State the blood parasite species.
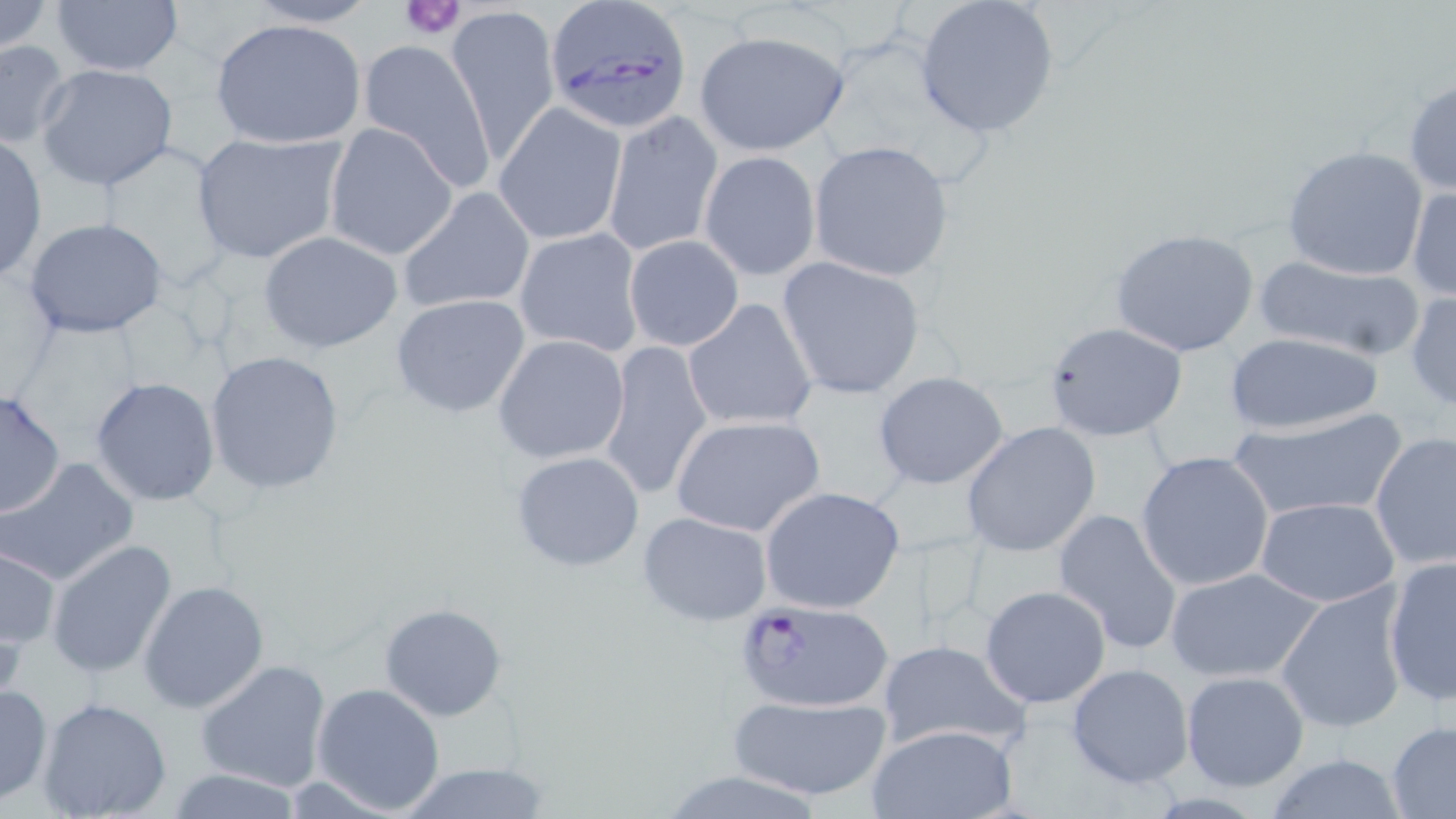

Plasmodium falciparum.

Approximate bounding boxes as named x1/y1/x2/y2 corners in pixels. Plasmodium falciparum-infected red blood cell locations: (x1=543, y1=2, x2=694, y2=133), (x1=732, y1=597, x2=896, y2=713). Platelet locations: (x1=400, y1=0, x2=467, y2=39). Uninfected red blood cell locations: (x1=0, y1=0, x2=56, y2=53), (x1=241, y1=0, x2=383, y2=28), (x1=913, y1=0, x2=1061, y2=139), (x1=49, y1=1, x2=184, y2=78), (x1=446, y1=5, x2=561, y2=163), (x1=208, y1=16, x2=365, y2=149), (x1=693, y1=29, x2=849, y2=157), (x1=0, y1=38, x2=74, y2=148), (x1=358, y1=39, x2=496, y2=190), (x1=36, y1=62, x2=181, y2=193), (x1=1403, y1=75, x2=1455, y2=198), (x1=495, y1=103, x2=626, y2=245), (x1=602, y1=110, x2=722, y2=256), (x1=324, y1=122, x2=458, y2=261), (x1=190, y1=131, x2=346, y2=265), (x1=0, y1=134, x2=48, y2=282), (x1=808, y1=140, x2=954, y2=282), (x1=1281, y1=145, x2=1429, y2=282), (x1=699, y1=151, x2=821, y2=280), (x1=1407, y1=183, x2=1455, y2=303), (x1=397, y1=186, x2=534, y2=316), (x1=23, y1=216, x2=171, y2=340), (x1=513, y1=228, x2=645, y2=356), (x1=1110, y1=228, x2=1262, y2=359), (x1=257, y1=230, x2=403, y2=353), (x1=623, y1=235, x2=744, y2=351), (x1=1251, y1=252, x2=1428, y2=362), (x1=776, y1=256, x2=927, y2=400), (x1=1406, y1=290, x2=1455, y2=413), (x1=390, y1=294, x2=531, y2=418), (x1=683, y1=298, x2=820, y2=432), (x1=1044, y1=322, x2=1186, y2=440), (x1=1223, y1=332, x2=1386, y2=437), (x1=493, y1=334, x2=631, y2=465), (x1=598, y1=339, x2=714, y2=500), (x1=203, y1=349, x2=344, y2=495), (x1=872, y1=372, x2=1011, y2=490), (x1=90, y1=377, x2=220, y2=505), (x1=0, y1=388, x2=66, y2=519), (x1=1230, y1=408, x2=1409, y2=523), (x1=669, y1=414, x2=826, y2=537), (x1=960, y1=421, x2=1102, y2=558), (x1=1370, y1=432, x2=1455, y2=575), (x1=510, y1=450, x2=646, y2=573), (x1=1135, y1=451, x2=1275, y2=592), (x1=2, y1=457, x2=139, y2=585), (x1=759, y1=486, x2=906, y2=615), (x1=1254, y1=496, x2=1401, y2=607), (x1=1051, y1=507, x2=1184, y2=655), (x1=638, y1=512, x2=773, y2=627), (x1=47, y1=538, x2=178, y2=680), (x1=1, y1=546, x2=60, y2=650), (x1=1382, y1=558, x2=1455, y2=708), (x1=1164, y1=566, x2=1326, y2=682), (x1=139, y1=580, x2=270, y2=714), (x1=1273, y1=583, x2=1409, y2=734), (x1=978, y1=584, x2=1110, y2=707), (x1=379, y1=602, x2=508, y2=721), (x1=876, y1=638, x2=1030, y2=752), (x1=194, y1=657, x2=333, y2=793), (x1=1065, y1=662, x2=1195, y2=788), (x1=1179, y1=670, x2=1309, y2=791), (x1=311, y1=681, x2=446, y2=815), (x1=0, y1=682, x2=51, y2=805), (x1=727, y1=693, x2=893, y2=802), (x1=36, y1=697, x2=173, y2=819), (x1=1386, y1=721, x2=1456, y2=817), (x1=863, y1=723, x2=1019, y2=819), (x1=1260, y1=754, x2=1414, y2=818), (x1=394, y1=763, x2=555, y2=819), (x1=165, y1=766, x2=305, y2=819), (x1=656, y1=769, x2=831, y2=819). One field of a larger specimen. Thin blood film. Light microscopy. May-Grünwald-Giemsa-stained preparation. Image is 1456×819 pixels. 1000x magnification.